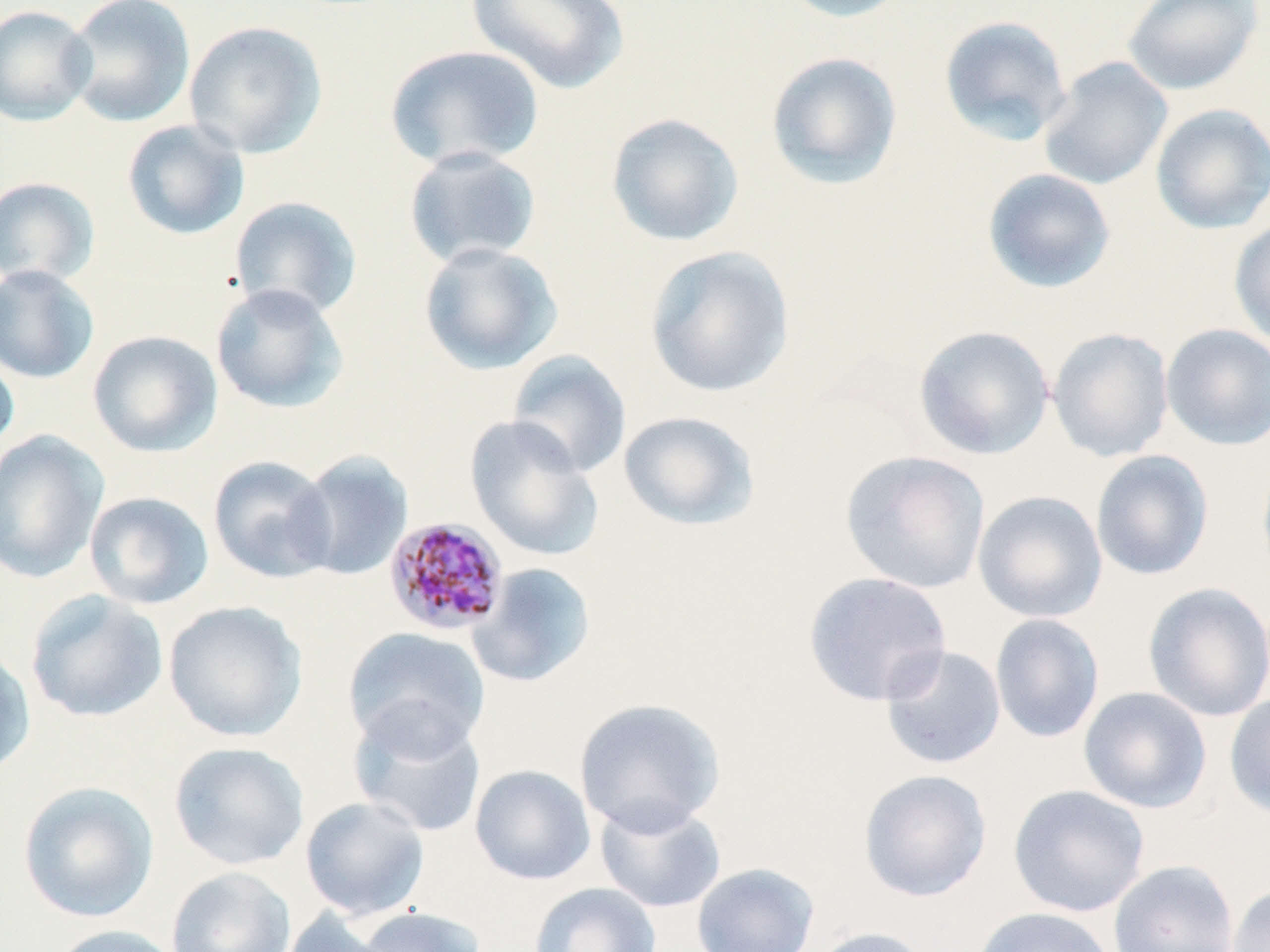
Approximate bounding boxes as (x1, y1, x2, y2) in pixels. Uninfected red blood cell locations: (63, 0, 196, 128), (465, 0, 630, 94), (774, 0, 913, 23), (1121, 0, 1263, 95), (0, 4, 96, 126), (939, 15, 1074, 146), (183, 20, 328, 159), (382, 44, 546, 171), (765, 51, 903, 191), (1038, 56, 1173, 191), (1150, 103, 1270, 235), (605, 112, 744, 247), (121, 119, 250, 241), (403, 146, 543, 269), (982, 168, 1116, 294), (0, 177, 100, 287), (229, 195, 363, 321), (1228, 218, 1270, 350), (417, 241, 563, 375), (644, 245, 796, 398), (0, 264, 100, 384), (210, 283, 349, 414), (1161, 323, 1270, 450), (913, 325, 1055, 460), (1047, 327, 1174, 463), (87, 330, 223, 457), (0, 348, 20, 458), (507, 350, 632, 479), (618, 410, 760, 531), (464, 416, 604, 562), (0, 430, 108, 584), (1090, 449, 1214, 581), (840, 450, 991, 594), (292, 451, 413, 581), (1256, 453, 1270, 584), (208, 455, 337, 584), (973, 490, 1107, 623), (83, 491, 214, 610), (467, 562, 597, 687), (802, 571, 953, 707), (1143, 582, 1270, 723), (25, 589, 169, 723), (163, 600, 307, 742), (990, 614, 1104, 744), (344, 626, 490, 758), (879, 645, 1006, 770), (0, 646, 36, 778), (1078, 686, 1212, 813), (1224, 693, 1270, 820), (573, 698, 726, 837), (348, 706, 486, 839), (168, 742, 310, 870), (470, 764, 595, 885), (857, 769, 992, 902), (17, 780, 159, 923), (1008, 784, 1150, 917), (300, 796, 430, 921), (595, 799, 726, 913), (1108, 859, 1240, 952), (692, 862, 819, 952), (166, 866, 297, 952), (528, 882, 661, 952), (1227, 884, 1270, 952), (355, 906, 487, 952), (971, 906, 1118, 952), (278, 907, 392, 952), (48, 924, 186, 952), (807, 926, 936, 952). Plasmodium malariae-infected red blood cell locations: (384, 516, 510, 636). Slide-level diagnosis: Plasmodium malariae. Image is 1270×952 pixels. May-Grünwald-Giemsa-stained preparation. 1000x magnification. Thin blood film. Single field of view. Optical microscopy.